Point out each leukocyte.
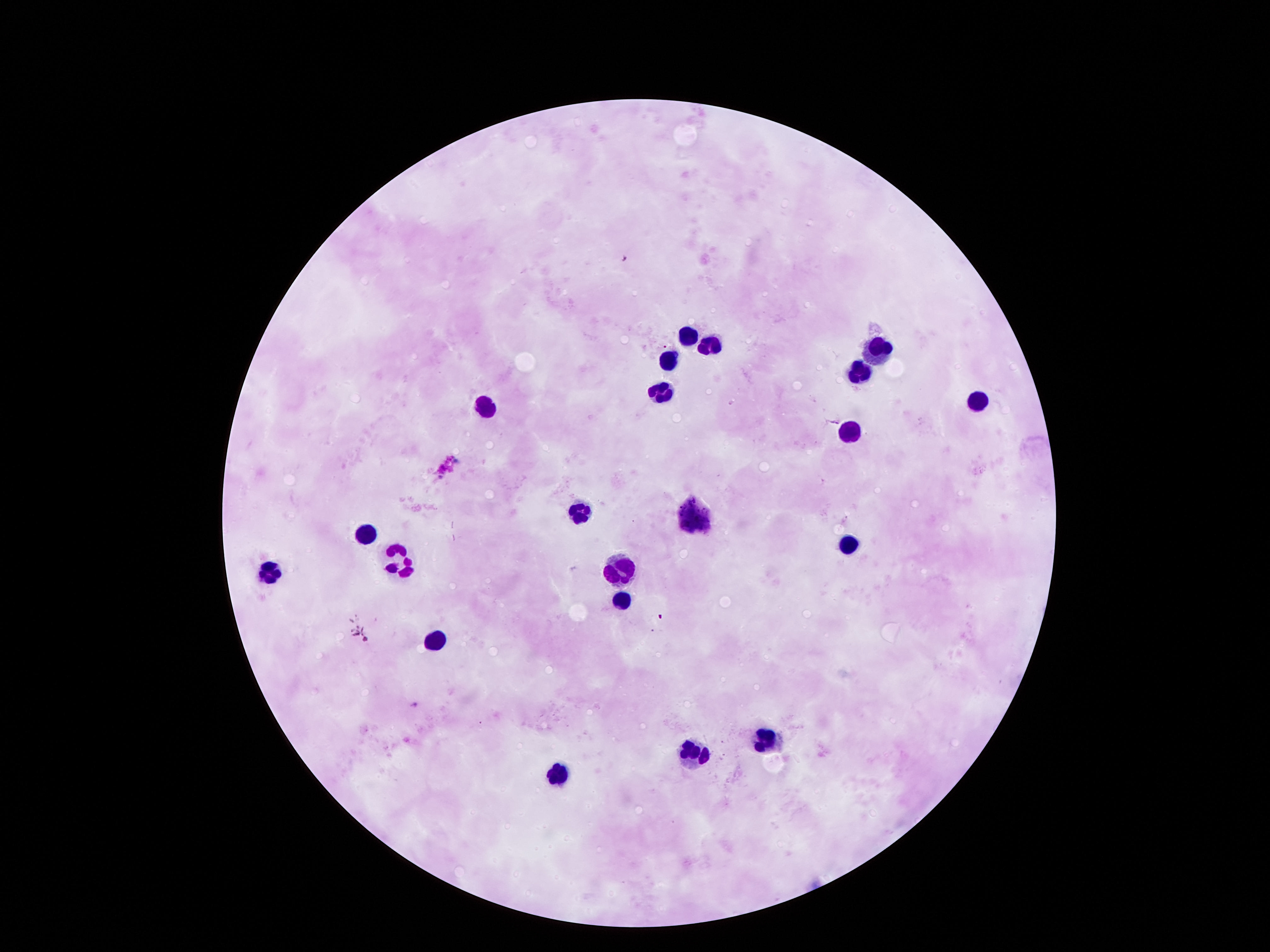
Approximate centers as {x, y} in pixels.
Leukocytes: {689, 333}, {707, 347}, {878, 351}, {668, 361}, {857, 372}, {663, 386}, {977, 397}, {486, 408}, {846, 430}, {585, 509}, {694, 509}, {363, 533}, {845, 545}, {401, 560}, {270, 568}, {621, 570}, {617, 601}, {431, 637}, {767, 733}, {697, 755}, {563, 773}.

Summary:
  - Preparation: thick blood film
  - Stain: Giemsa
  - Image size: 1270×952 pixels
  - Field of view: single
  - Magnification: 100x
  - Capture: smartphone camera through the microscope eyepiece
  - Patient malaria status: negative